Assess this cell for malaria.
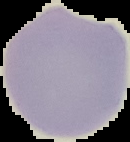
Uninfected.

Segmented cell region on a black background. From a thin blood smear. Image is 130×142 pixels.